Outline each Plasmodium ovale-infected red blood cell.
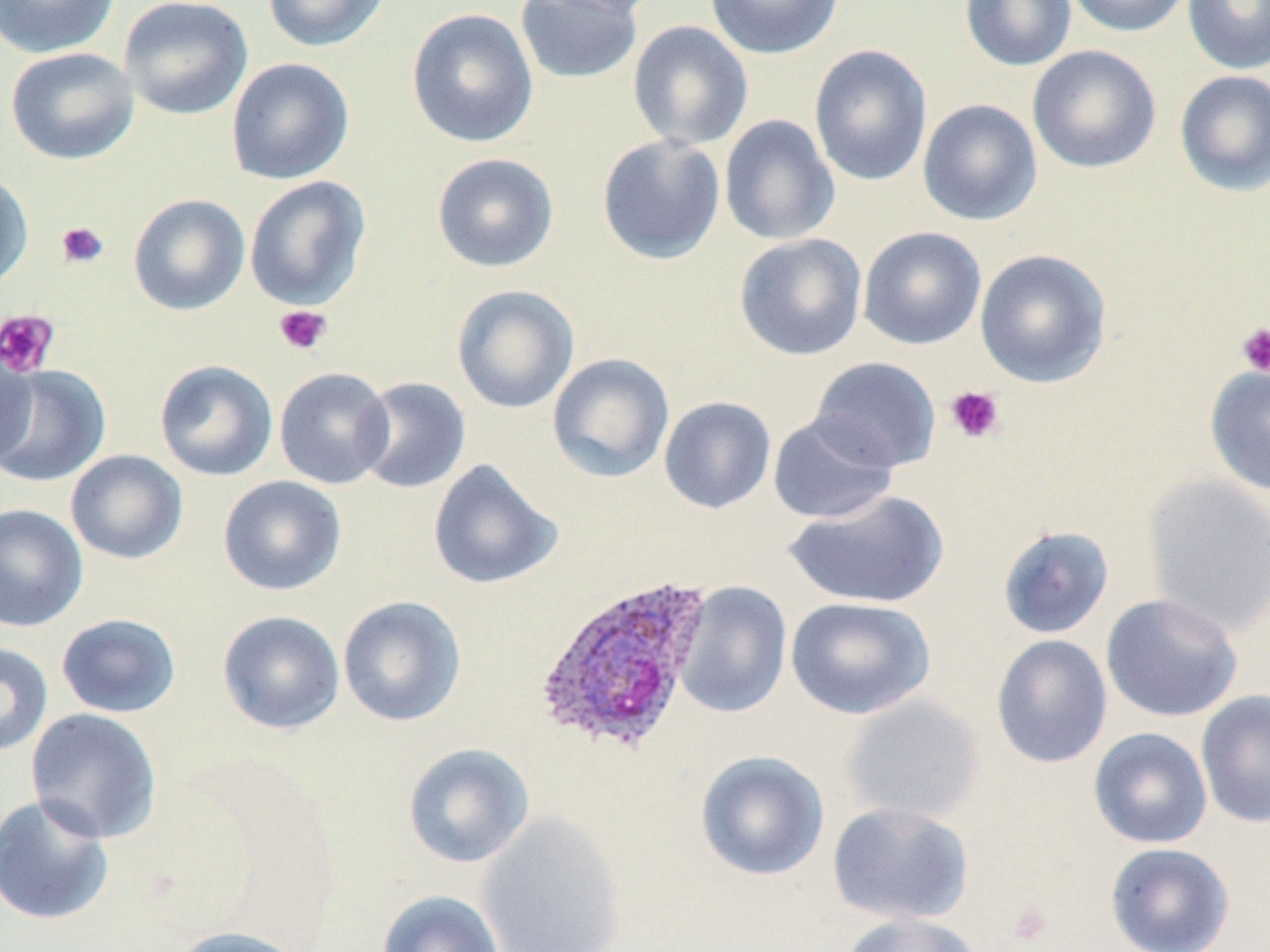
Approximate bounding boxes as (x1,y1)-(x2,y2) corner pairs in pixels.
Plasmodium ovale-infected red blood cells: (533,574)-(713,756).

slide_level_diagnosis: Plasmodium ovale
field_of_view: one of a larger specimen
modality: optical microscopy
preparation: thin blood film
magnification: 1000x
platelet_locations: 'approximate bounding boxes as (x1,y1)-(x2,y2) corner pairs in pixels: (56,221)-(109,269), (273,305)-(332,356), (0,309)-(59,378), (1236,322)-(1270,378), (945,385)-(1006,444), (1009,901)-(1052,946)'
image_size: 1270×952 pixels
uninfected_red_blood_cell_locations: 'approximate bounding boxes as (x1,y1)-(x2,y2) corner pairs in pixels: (0,0)-(120,59), (119,0)-(254,120), (261,0)-(389,53), (529,0)-(663,19), (704,0)-(843,60), (960,0)-(1077,71), (1064,0)-(1192,37), (1182,0)-(1270,74), (514,1)-(643,85), (406,8)-(538,147), (627,20)-(754,151), (808,44)-(933,187), (1026,44)-(1162,174), (5,47)-(140,165), (226,58)-(355,185), (1174,70)-(1270,197), (917,98)-(1042,226), (719,114)-(840,246), (596,134)-(726,265), (431,152)-(559,273), (0,170)-(33,293), (244,175)-(371,311), (128,193)-(250,316), (858,226)-(987,350), (733,233)-(867,361), (974,248)-(1112,388), (451,284)-(579,414), (0,343)-(36,470), (547,353)-(674,483), (809,356)-(941,472), (154,360)-(278,482), (0,364)-(111,488), (1204,364)-(1270,497), (274,366)-(395,489), (355,376)-(471,494), (658,396)-(776,514), (767,413)-(898,524), (65,449)-(188,565), (428,459)-(561,590), (1141,473)-(1270,636), (218,475)-(347,596), (783,489)-(949,609), (0,503)-(87,632), (996,525)-(1114,640), (673,581)-(793,718), (1100,593)-(1243,723), (337,595)-(467,727), (786,596)-(936,720), (217,610)-(345,734), (55,613)-(181,718), (991,634)-(1113,769), (0,642)-(53,757), (1195,689)-(1270,828), (840,694)-(985,824), (25,708)-(162,843), (1088,727)-(1213,849), (402,743)-(534,868), (695,750)-(830,881), (0,792)-(115,926), (826,801)-(974,925), (476,812)-(627,952), (1104,842)-(1235,951), (377,890)-(505,952), (838,912)-(982,952), (169,925)-(308,952)'
stain: May-Grünwald-Giemsa